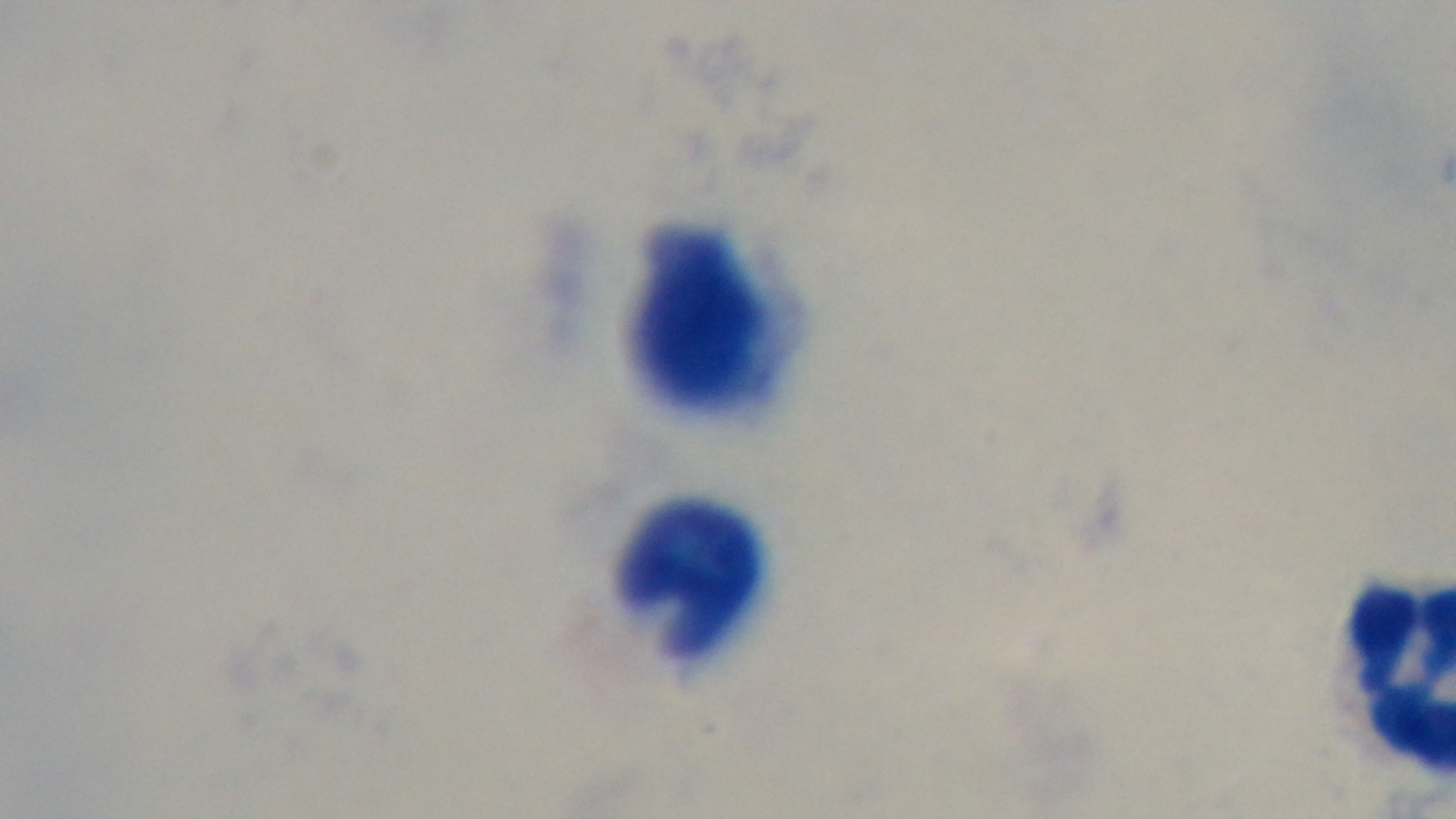

{
  "objective": "100x oil immersion",
  "capture": "mounted 4K digital camera",
  "field_of_view": "one from the slide",
  "malaria_status": "negative",
  "preparation": "thick",
  "stain": "Giemsa",
  "modality": "light microscopy"
}